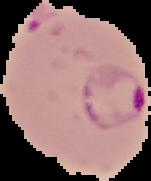

Malaria status: parasitized. From a thin blood smear. Image is 151×181 pixels. Segmented cell region on a black background.